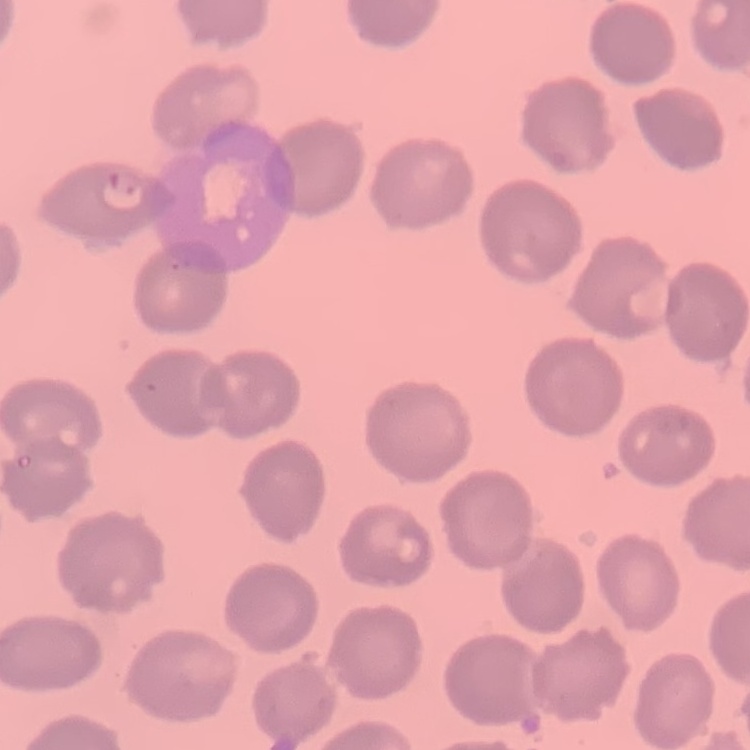

erythrocyte morphology = no rouleaux formation
stain = Field's or Giemsa
image type = square crop of a larger photomicrograph
preparation = thin blood film